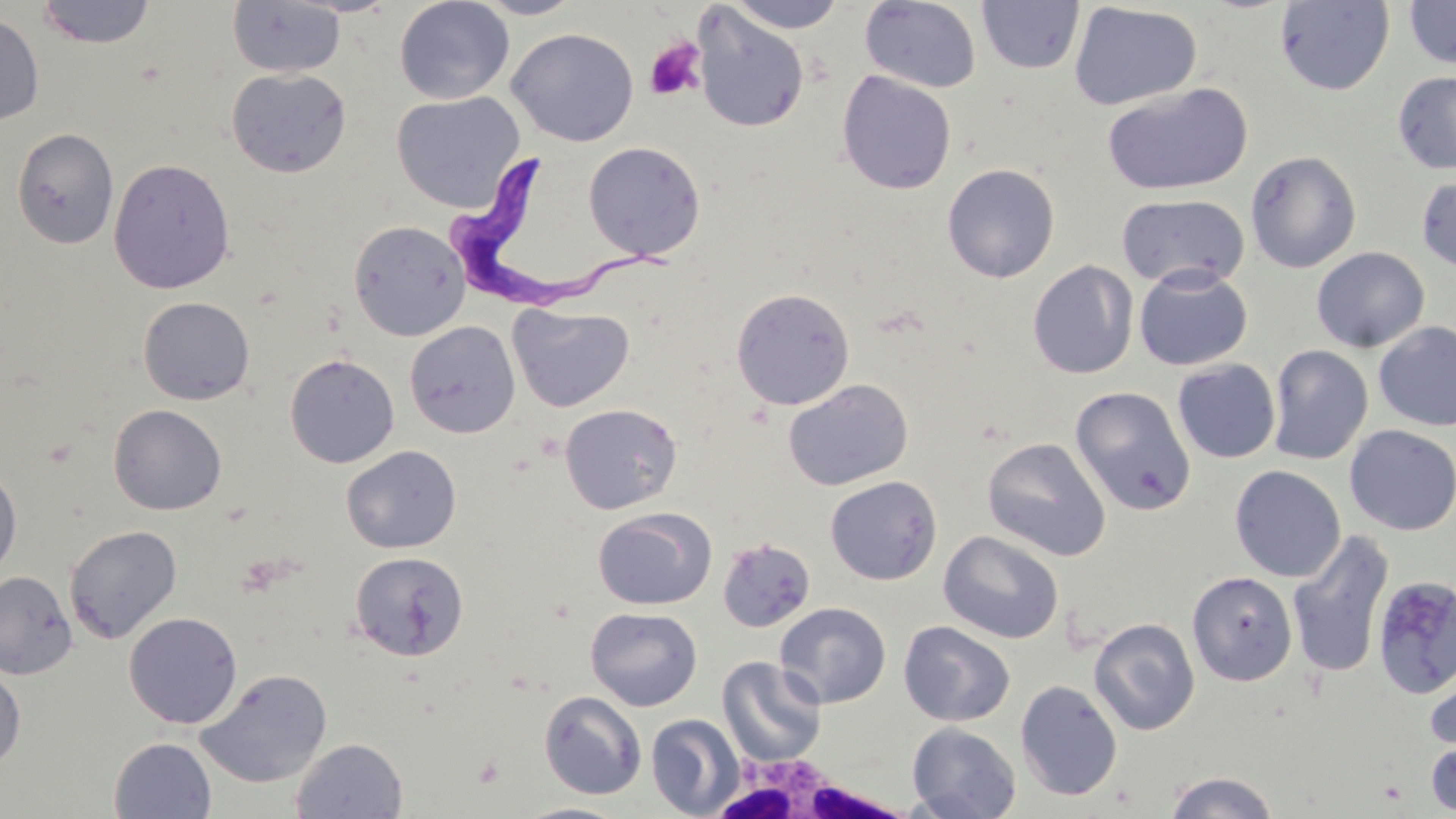

Summary:
  - Coordinate format: approximate bounding boxes as (x1,y1)-(x2,y2) corner pairs in pixels
  - Trypanosoma brucei locations: (445,153)-(676,316)
  - Uninfected red blood cell locations: (36,0)-(156,49), (394,0)-(514,105), (472,0)-(584,20), (725,0)-(847,33), (976,0)-(1085,74), (227,1)-(346,78), (860,1)-(982,93), (1274,1)-(1395,95), (1403,1)-(1456,69), (1068,2)-(1202,111), (691,6)-(809,133), (0,11)-(44,127), (506,27)-(639,146), (226,68)-(351,178), (837,70)-(957,195), (1392,71)-(1456,175), (1102,82)-(1253,196), (391,91)-(525,210), (11,128)-(119,248), (582,141)-(706,261), (1245,150)-(1362,273), (108,157)-(235,294), (941,163)-(1060,283), (1416,174)-(1456,273), (1116,193)-(1250,289), (348,219)-(471,341), (1311,247)-(1429,353), (1027,260)-(1138,379), (1134,266)-(1252,371), (731,287)-(855,410), (137,296)-(255,405), (508,304)-(634,412), (404,320)-(521,439), (1373,321)-(1456,431), (1267,344)-(1373,465), (284,353)-(400,468), (1173,359)-(1281,463), (783,379)-(913,491), (1070,385)-(1196,515), (559,403)-(682,515), (108,404)-(227,515), (1344,424)-(1456,535), (982,438)-(1110,561), (341,445)-(461,554), (0,460)-(22,580), (1229,465)-(1346,582), (825,475)-(942,585), (592,507)-(716,610), (64,524)-(182,644), (1287,529)-(1395,679), (938,530)-(1064,644), (716,537)-(816,634), (349,551)-(468,661), (0,570)-(77,680), (1187,571)-(1298,686), (1372,575)-(1456,698), (774,602)-(891,708), (585,607)-(702,711), (123,611)-(243,729), (1088,617)-(1200,736), (898,620)-(1016,727), (717,656)-(827,767), (1424,660)-(1456,762), (0,664)-(26,772), (195,668)-(332,788), (1015,678)-(1123,801), (539,690)-(647,800), (646,714)-(745,818), (907,721)-(1021,819), (1425,736)-(1456,816), (109,737)-(217,818), (291,737)-(408,818), (1164,771)-(1281,818), (511,801)-(635,819)
  - Platelet locations: (644,38)-(707,101)
  - White blood cell locations: (712,747)-(902,819)
  - Slide-level diagnosis: Trypanosoma brucei
  - Magnification: 1000x
  - Stain: May-Grünwald-Giemsa
  - Modality: optical microscopy
  - Image size: 1456×819 pixels
  - Preparation: thin blood film
  - Field of view: single